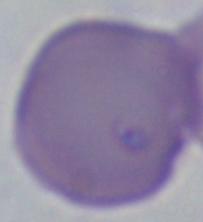
Summary:
  - Magnification: 1000x
  - Modality: photomicrograph
  - Identification: Babesia